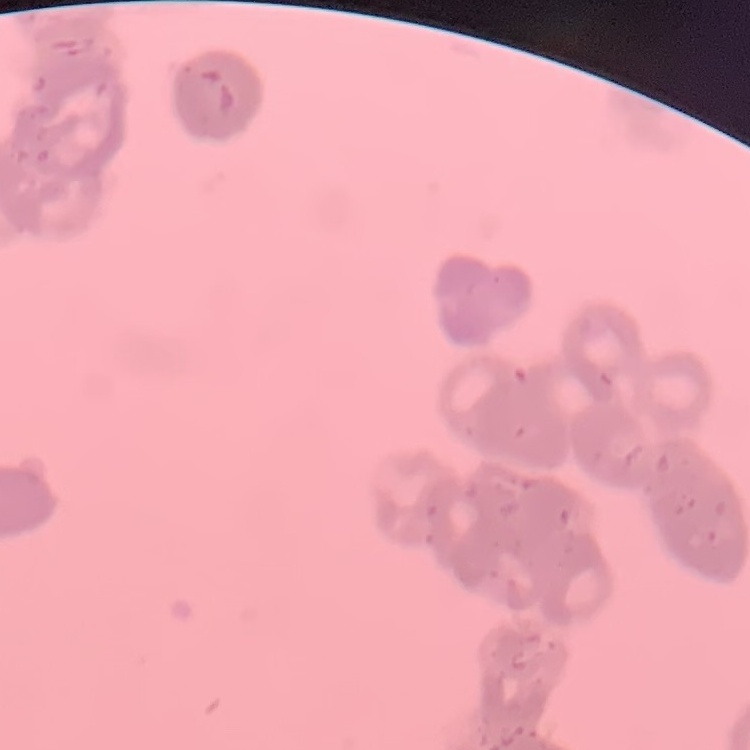 The erythrocytes show rouleaux formation. Thin blood smear. One tile cut from a larger photomicrograph. Stained with either Field's or Giemsa.